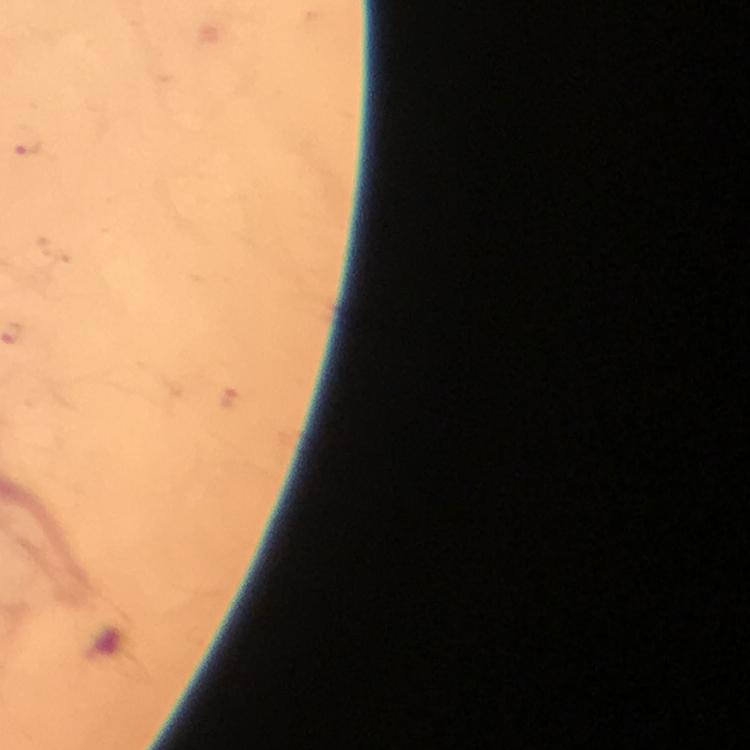
Approximate centers as (x, y) in pixels. Malaria parasite locations: (23, 140). At 100x magnification. Image is 750×750 pixels. Thick smear. Giemsa-stained preparation. Smartphone photograph taken through a microscope. From a malaria diagnostic workup. A crop from one field of view. Immersion oil was used.